Classify this cell by malaria status.
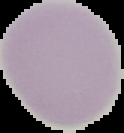
It is uninfected.

preparation = thin blood smear
image type = segmented cell region with the area outside set to black
image size = 124×133 pixels